Comment on the morphology of the red blood cells.
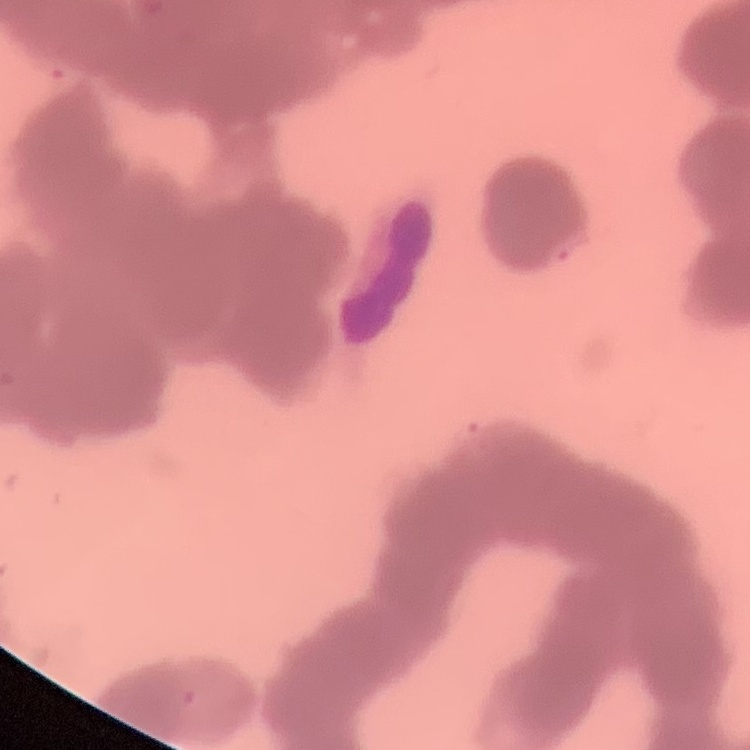

They show rouleaux formation.

Thin blood smear. Field's or Giemsa stain. Square crop of a larger photomicrograph.